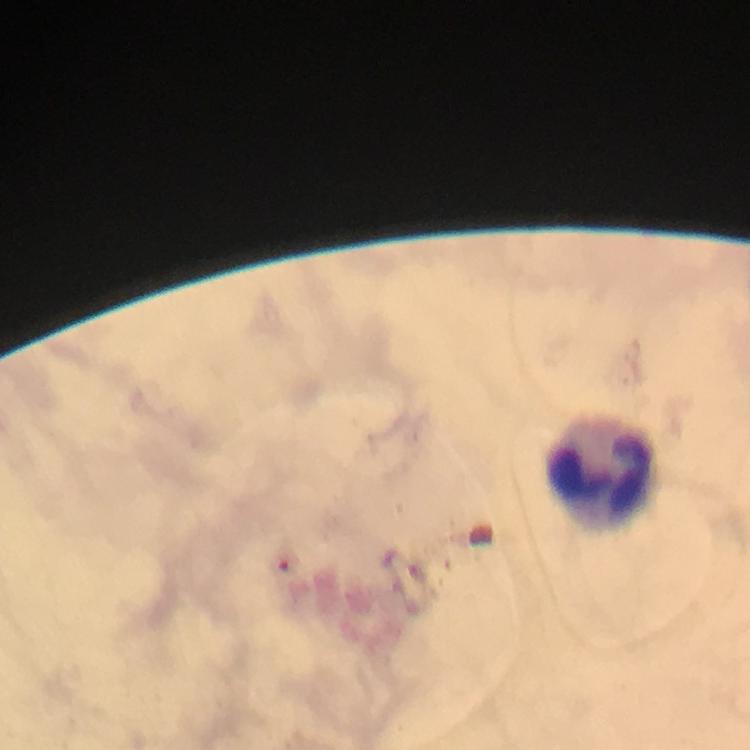
capture = smartphone photograph through a microscope
leukocyte locations = approximate object centers, in pixels from the top-left corner: (x=602, y=470)
stain = Giemsa
malaria parasites = none seen
image size = 750×750 pixels
context = from a diagnostic examination for malaria
magnification = 100x
preparation = thick blood film
immersion oil = applied
cropped from = a single field of view